Locate every Plasmodium parasite.
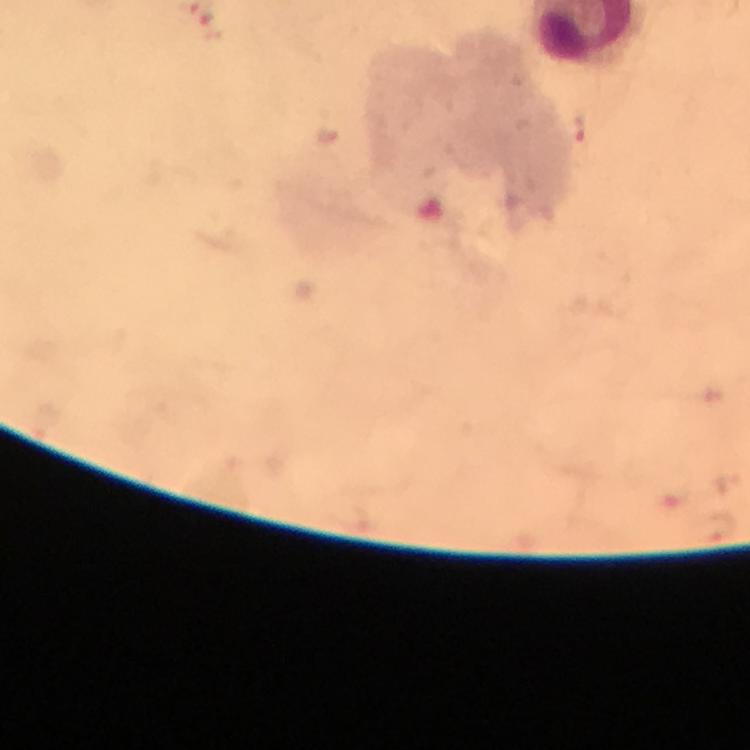

Approximate centers as [x, y] in pixels.
Plasmodium parasites: [583, 127].

Cropped region of a single field of view. Giemsa-stained preparation. From a malaria diagnostic workup. Smartphone photograph taken through a microscope. Immersion oil was used. Image is 750×750 pixels. Thick blood smear. 100x magnification.